Name the blood parasite species.
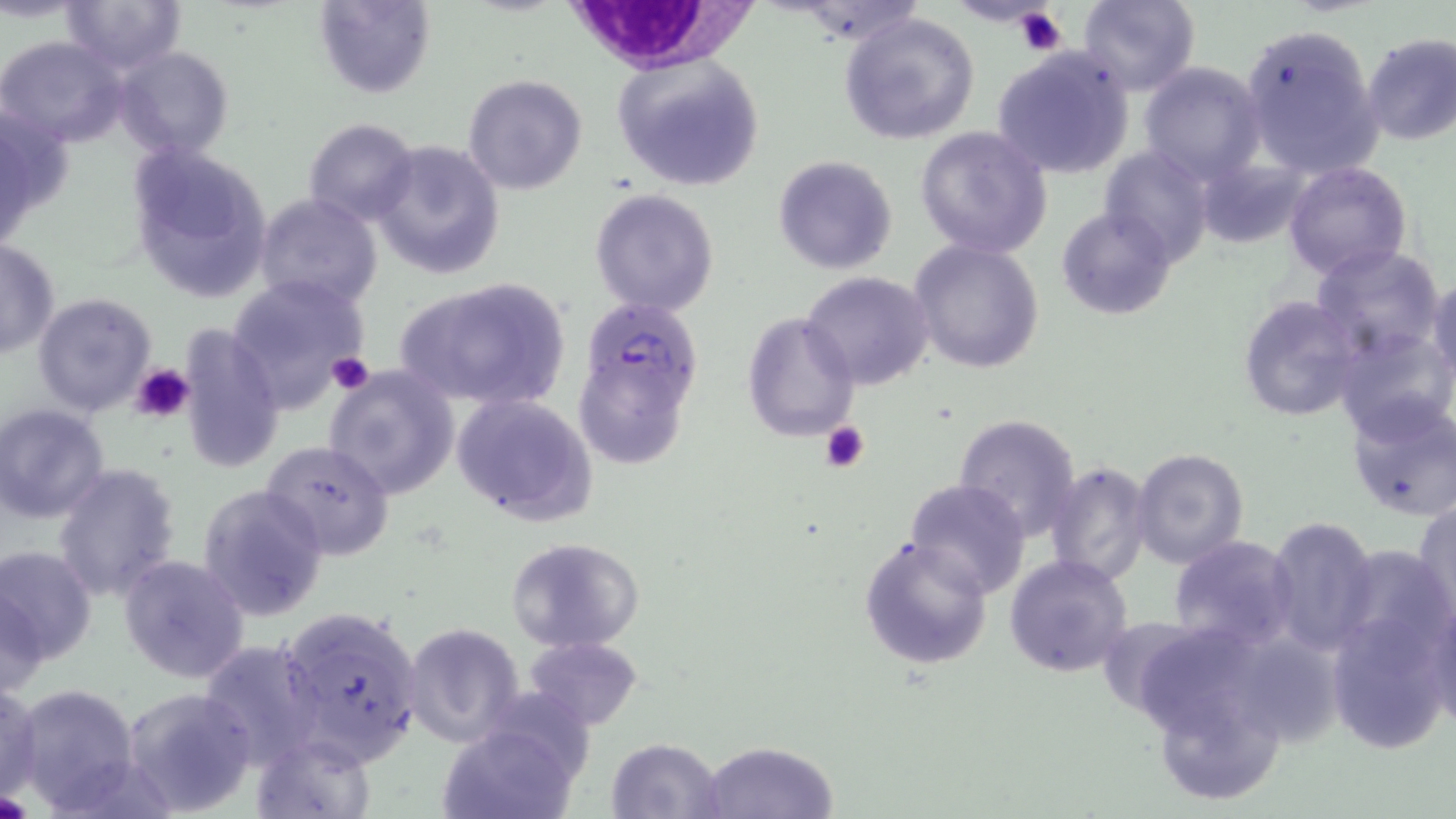

Plasmodium falciparum.

Approximate bounding boxes as [x1, y1, x2, y2] in pixels. Plasmodium falciparum-infected red blood cell locations: [572, 294, 704, 412]. Platelet locations: [1016, 8, 1068, 56], [327, 351, 374, 396], [132, 363, 193, 424], [820, 420, 869, 474], [0, 791, 29, 818]. Uninfected red blood cell locations: [61, 0, 184, 72], [313, 0, 435, 99], [1076, 0, 1202, 96], [838, 11, 980, 144], [1239, 22, 1384, 179], [1361, 32, 1456, 146], [0, 36, 127, 148], [112, 46, 235, 163], [991, 48, 1137, 179], [612, 54, 765, 192], [1139, 62, 1268, 186], [463, 73, 588, 195], [0, 100, 70, 251], [301, 118, 420, 228], [915, 127, 1054, 258], [370, 139, 507, 280], [128, 143, 273, 303], [1100, 147, 1213, 269], [773, 154, 898, 275], [1199, 156, 1306, 246], [1282, 159, 1412, 283], [144, 175, 388, 307], [590, 187, 721, 317], [254, 193, 382, 310], [1057, 207, 1176, 320], [0, 238, 59, 359], [909, 239, 1045, 372], [1309, 244, 1446, 362], [801, 270, 935, 390], [225, 274, 370, 414], [393, 275, 569, 413], [1427, 276, 1456, 388], [31, 291, 158, 419], [1237, 295, 1365, 423], [741, 311, 860, 442], [175, 321, 285, 477], [1333, 323, 1454, 443], [322, 365, 461, 501], [579, 367, 689, 467], [1343, 392, 1456, 521], [452, 393, 598, 526], [0, 403, 109, 523], [953, 412, 1082, 542], [262, 440, 396, 561], [1131, 448, 1249, 569], [53, 461, 182, 602], [1044, 461, 1153, 587], [904, 478, 1032, 597], [197, 483, 330, 621], [1412, 501, 1455, 621], [1265, 516, 1377, 655], [858, 534, 995, 670], [1167, 536, 1299, 656], [504, 537, 646, 653], [0, 543, 98, 667], [1336, 545, 1450, 666], [119, 554, 250, 684], [1004, 555, 1132, 678], [1, 578, 47, 700], [1424, 593, 1456, 733], [277, 604, 425, 769], [1324, 615, 1451, 754], [404, 623, 526, 748], [1141, 633, 1262, 741], [525, 635, 644, 731], [198, 639, 326, 769], [12, 683, 141, 813], [1162, 684, 1286, 799], [0, 685, 44, 803], [123, 686, 259, 816], [439, 722, 579, 819], [250, 732, 378, 819], [606, 737, 726, 819], [700, 740, 839, 818]. White blood cell locations: [567, 4, 764, 84]. One field of a larger specimen. 1000x magnification. Thin blood smear. Light microscopy. Image is 1456×819 pixels. May-Grünwald-Giemsa-stained preparation.